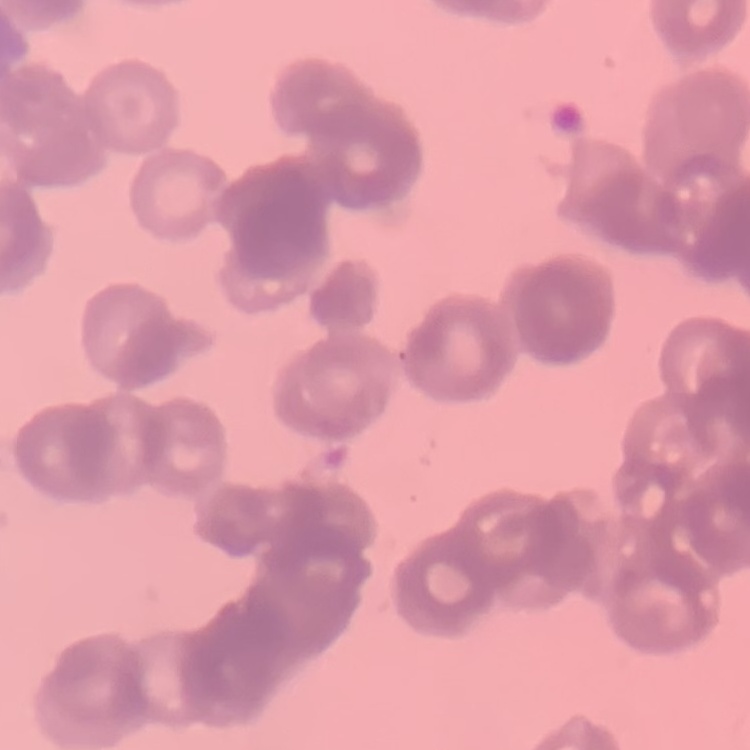

Summary:
  - Red blood cell morphology: rouleaux formation
  - Image type: one tile cut from a larger photomicrograph
  - Stain: Field's or Giemsa
  - Preparation: thin blood smear